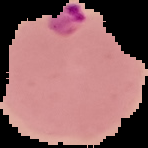

{
  "result": "Plasmodium parasites detected",
  "image_size": "148×148 pixels",
  "image_type": "segmented cell region on a black background",
  "preparation": "thin blood smear"
}